Assess this cell for malaria.
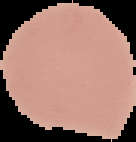
Uninfected.

Summary:
  - Preparation: thin blood film
  - Image type: segmented cell region with the area outside set to black
  - Image size: 136×142 pixels